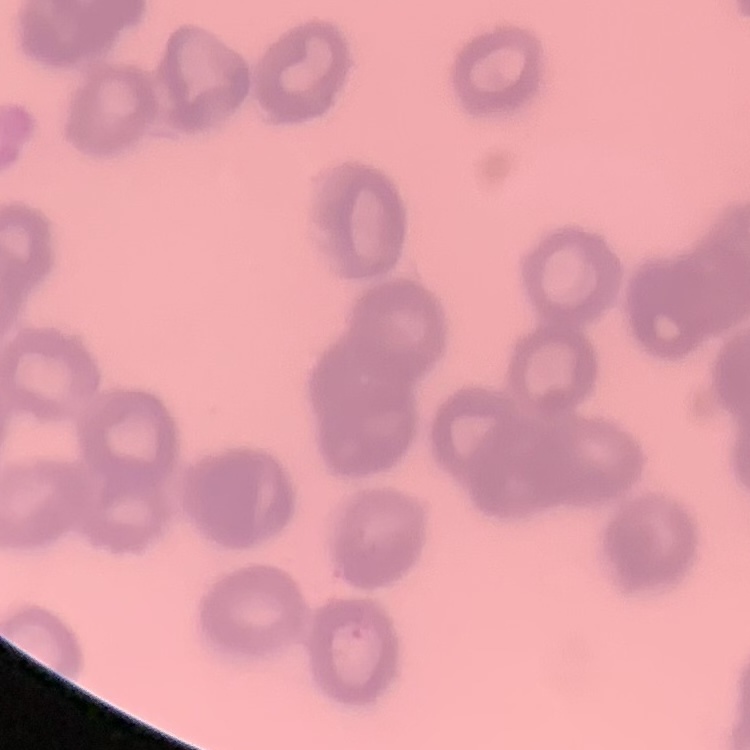

erythrocyte morphology = rouleaux formation
stain = Field's or Giemsa
image type = square crop of a larger photomicrograph
preparation = thin blood film